Locate every uninfected red blood cell.
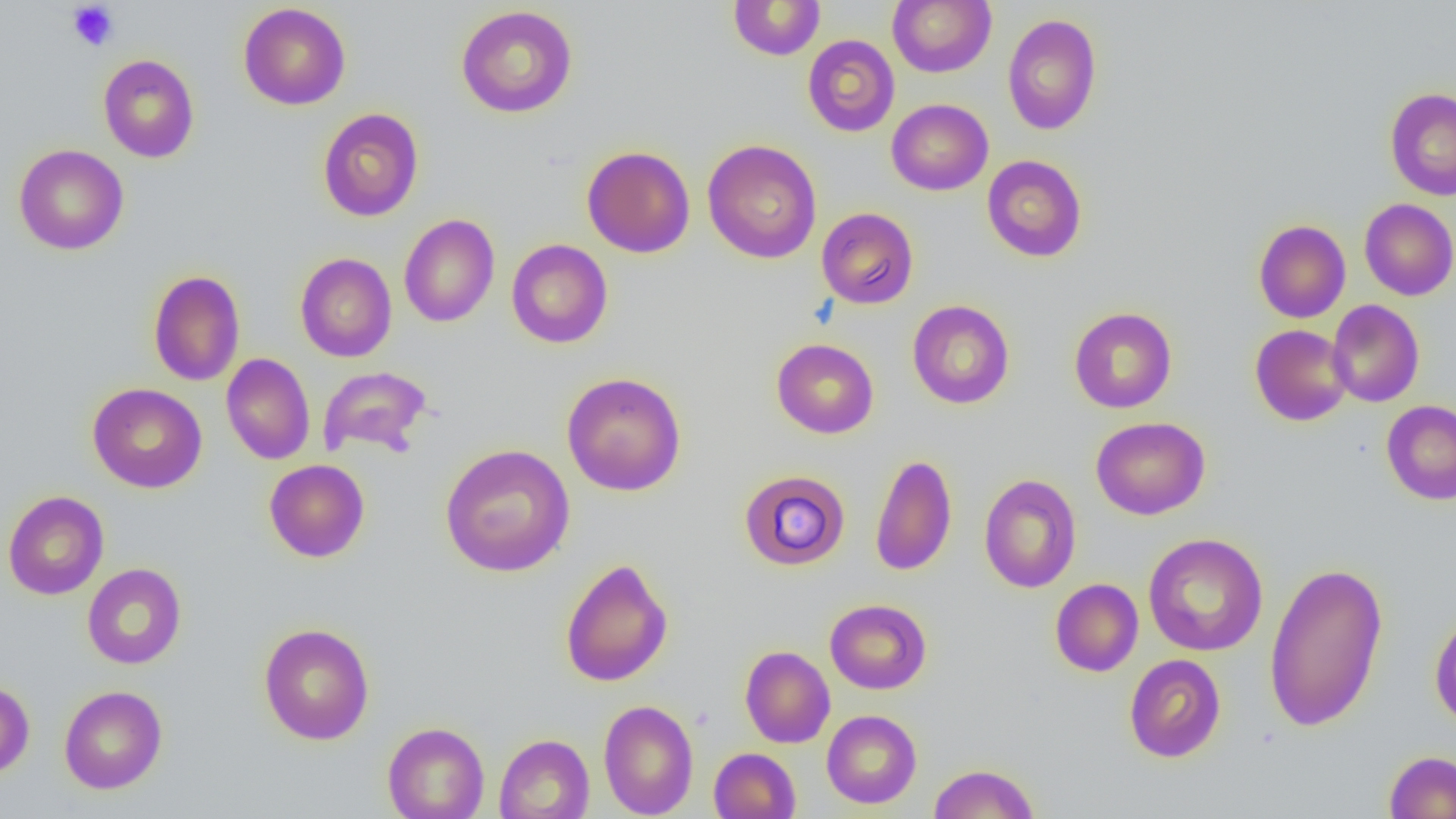
Approximate bounding boxes as named x1/y1/x2/y2 corners in pixels.
Uninfected red blood cells: (x1=888, y1=0, x2=996, y2=77), (x1=728, y1=1, x2=826, y2=60), (x1=238, y1=3, x2=351, y2=110), (x1=456, y1=5, x2=578, y2=118), (x1=1003, y1=14, x2=1101, y2=135), (x1=802, y1=34, x2=900, y2=137), (x1=98, y1=54, x2=200, y2=163), (x1=1385, y1=88, x2=1456, y2=200), (x1=887, y1=99, x2=993, y2=195), (x1=317, y1=108, x2=424, y2=222), (x1=703, y1=139, x2=822, y2=264), (x1=13, y1=143, x2=129, y2=255), (x1=582, y1=145, x2=695, y2=258), (x1=982, y1=155, x2=1087, y2=262), (x1=1359, y1=198, x2=1456, y2=300), (x1=816, y1=207, x2=919, y2=309), (x1=399, y1=213, x2=499, y2=328), (x1=1253, y1=219, x2=1351, y2=323), (x1=506, y1=239, x2=613, y2=348), (x1=295, y1=253, x2=397, y2=362), (x1=148, y1=269, x2=245, y2=386), (x1=907, y1=300, x2=1015, y2=409), (x1=1327, y1=300, x2=1425, y2=407), (x1=1069, y1=307, x2=1177, y2=413), (x1=1250, y1=324, x2=1353, y2=426), (x1=771, y1=338, x2=879, y2=438), (x1=221, y1=353, x2=315, y2=465), (x1=317, y1=365, x2=433, y2=460), (x1=562, y1=372, x2=686, y2=496), (x1=87, y1=383, x2=207, y2=493), (x1=1381, y1=400, x2=1456, y2=505), (x1=1090, y1=416, x2=1210, y2=520), (x1=440, y1=443, x2=575, y2=577), (x1=869, y1=453, x2=957, y2=577), (x1=264, y1=459, x2=370, y2=562), (x1=739, y1=469, x2=850, y2=571), (x1=978, y1=474, x2=1082, y2=593), (x1=2, y1=490, x2=109, y2=600), (x1=1142, y1=533, x2=1268, y2=656), (x1=560, y1=557, x2=673, y2=687), (x1=1264, y1=561, x2=1388, y2=733), (x1=82, y1=563, x2=186, y2=669), (x1=1050, y1=578, x2=1143, y2=676), (x1=824, y1=599, x2=931, y2=694), (x1=1429, y1=610, x2=1456, y2=729), (x1=258, y1=622, x2=375, y2=745), (x1=739, y1=645, x2=835, y2=748), (x1=1124, y1=654, x2=1226, y2=763), (x1=0, y1=680, x2=34, y2=779), (x1=59, y1=685, x2=167, y2=794), (x1=598, y1=699, x2=699, y2=818), (x1=821, y1=709, x2=921, y2=809), (x1=382, y1=721, x2=489, y2=819), (x1=494, y1=733, x2=594, y2=819), (x1=709, y1=747, x2=801, y2=819), (x1=1384, y1=750, x2=1456, y2=818), (x1=928, y1=763, x2=1040, y2=818).

Summary:
  - Platelet locations: (x1=67, y1=2, x2=119, y2=51)
  - Slide-level diagnosis: negative for blood parasites
  - Modality: optical microscopy
  - Image size: 1456×819 pixels
  - Preparation: thin blood film
  - Magnification: 1000x
  - Field of view: one of a larger specimen